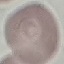

Summary:
  - Result: no malaria parasites seen
  - Capture: smartphone camera at the microscope eyepiece
  - Stain: Giemsa
  - Image type: automatically extracted cell patch, resized to 64 × 64 pixels
  - Preparation: thin smear